Locate every blood parasite and identify its species.
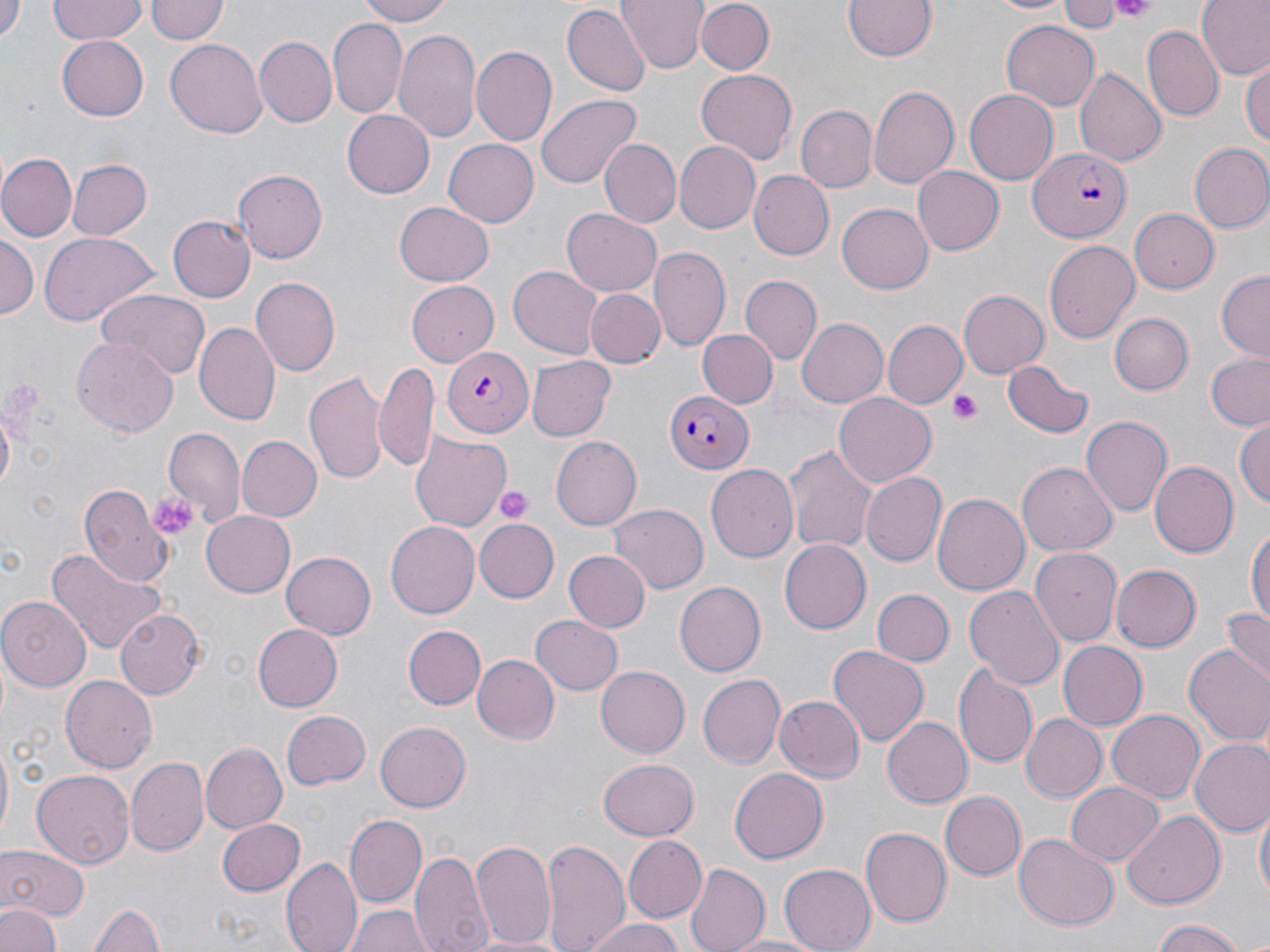
Approximate bounding boxes as named x1/y1/x2/y2 corners in pixels.
Plasmodium falciparum-infected red blood cells: (x1=1030, y1=149, x2=1130, y2=240), (x1=440, y1=349, x2=532, y2=436), (x1=661, y1=387, x2=753, y2=474).
No Plasmodium ovale, Plasmodium malariae, Plasmodium vivax, Babesia divergens, or Trypanosoma brucei observed.

Summary:
  - Uninfected red blood cell locations: (x1=0, y1=0, x2=23, y2=45), (x1=49, y1=0, x2=147, y2=44), (x1=145, y1=0, x2=226, y2=45), (x1=355, y1=0, x2=459, y2=26), (x1=617, y1=0, x2=705, y2=74), (x1=841, y1=0, x2=940, y2=63), (x1=980, y1=0, x2=1078, y2=15), (x1=1197, y1=0, x2=1269, y2=79), (x1=696, y1=1, x2=775, y2=74), (x1=1058, y1=1, x2=1122, y2=30), (x1=561, y1=5, x2=649, y2=95), (x1=330, y1=20, x2=406, y2=116), (x1=1001, y1=21, x2=1102, y2=110), (x1=1141, y1=25, x2=1225, y2=123), (x1=393, y1=28, x2=481, y2=144), (x1=56, y1=32, x2=149, y2=118), (x1=253, y1=36, x2=336, y2=126), (x1=165, y1=39, x2=266, y2=139), (x1=470, y1=45, x2=558, y2=146), (x1=1241, y1=61, x2=1269, y2=144), (x1=695, y1=68, x2=797, y2=163), (x1=1075, y1=68, x2=1166, y2=168), (x1=868, y1=85, x2=959, y2=190), (x1=963, y1=89, x2=1059, y2=184), (x1=536, y1=94, x2=643, y2=188), (x1=795, y1=106, x2=875, y2=194), (x1=341, y1=109, x2=434, y2=198), (x1=444, y1=137, x2=542, y2=227), (x1=599, y1=139, x2=681, y2=228), (x1=674, y1=141, x2=761, y2=232), (x1=1188, y1=143, x2=1270, y2=234), (x1=1, y1=155, x2=77, y2=240), (x1=66, y1=159, x2=151, y2=240), (x1=913, y1=167, x2=1003, y2=255), (x1=232, y1=169, x2=326, y2=264), (x1=748, y1=170, x2=834, y2=260), (x1=391, y1=201, x2=494, y2=286), (x1=836, y1=203, x2=932, y2=294), (x1=562, y1=208, x2=663, y2=296), (x1=1129, y1=208, x2=1219, y2=293), (x1=169, y1=215, x2=256, y2=301), (x1=39, y1=232, x2=158, y2=326), (x1=0, y1=233, x2=38, y2=320), (x1=1044, y1=239, x2=1140, y2=345), (x1=651, y1=247, x2=731, y2=351), (x1=509, y1=263, x2=604, y2=358), (x1=1216, y1=272, x2=1269, y2=360), (x1=740, y1=274, x2=822, y2=362), (x1=249, y1=275, x2=340, y2=379), (x1=406, y1=280, x2=499, y2=365), (x1=584, y1=288, x2=666, y2=368), (x1=99, y1=289, x2=209, y2=379), (x1=958, y1=289, x2=1050, y2=377), (x1=1109, y1=312, x2=1192, y2=394), (x1=797, y1=319, x2=888, y2=406), (x1=884, y1=321, x2=967, y2=408), (x1=195, y1=322, x2=280, y2=426), (x1=696, y1=329, x2=778, y2=409), (x1=71, y1=335, x2=179, y2=438), (x1=1205, y1=353, x2=1270, y2=431), (x1=528, y1=357, x2=614, y2=440), (x1=1001, y1=359, x2=1095, y2=439), (x1=375, y1=362, x2=435, y2=473), (x1=305, y1=369, x2=389, y2=483), (x1=833, y1=391, x2=936, y2=488), (x1=1082, y1=416, x2=1172, y2=517), (x1=1234, y1=418, x2=1270, y2=512), (x1=165, y1=429, x2=244, y2=527), (x1=410, y1=431, x2=511, y2=530), (x1=236, y1=435, x2=320, y2=521), (x1=549, y1=436, x2=642, y2=530), (x1=784, y1=443, x2=877, y2=554), (x1=1150, y1=460, x2=1239, y2=557), (x1=1017, y1=463, x2=1117, y2=555), (x1=708, y1=466, x2=799, y2=562), (x1=862, y1=472, x2=945, y2=565), (x1=76, y1=482, x2=169, y2=587), (x1=931, y1=492, x2=1030, y2=595), (x1=609, y1=505, x2=707, y2=593), (x1=200, y1=508, x2=296, y2=595), (x1=473, y1=517, x2=559, y2=602), (x1=386, y1=521, x2=480, y2=617), (x1=1246, y1=526, x2=1270, y2=632), (x1=780, y1=541, x2=871, y2=633), (x1=46, y1=546, x2=167, y2=657), (x1=1031, y1=547, x2=1122, y2=646), (x1=281, y1=550, x2=376, y2=638), (x1=565, y1=552, x2=649, y2=632), (x1=1111, y1=567, x2=1199, y2=651), (x1=675, y1=581, x2=765, y2=677), (x1=963, y1=583, x2=1064, y2=687), (x1=870, y1=588, x2=954, y2=667), (x1=0, y1=595, x2=91, y2=688), (x1=1222, y1=606, x2=1270, y2=685), (x1=115, y1=609, x2=205, y2=699), (x1=531, y1=614, x2=623, y2=694), (x1=254, y1=624, x2=342, y2=711), (x1=402, y1=624, x2=484, y2=711), (x1=1058, y1=639, x2=1146, y2=732), (x1=828, y1=645, x2=929, y2=746), (x1=1185, y1=645, x2=1270, y2=748), (x1=471, y1=654, x2=558, y2=744), (x1=954, y1=662, x2=1036, y2=769), (x1=595, y1=663, x2=689, y2=756), (x1=697, y1=674, x2=783, y2=770), (x1=62, y1=675, x2=159, y2=774), (x1=774, y1=695, x2=863, y2=783), (x1=281, y1=709, x2=369, y2=789), (x1=1107, y1=710, x2=1206, y2=803), (x1=1020, y1=714, x2=1108, y2=803), (x1=882, y1=716, x2=971, y2=808), (x1=375, y1=720, x2=470, y2=811), (x1=0, y1=740, x2=13, y2=844), (x1=1190, y1=740, x2=1270, y2=838), (x1=200, y1=743, x2=287, y2=834), (x1=127, y1=756, x2=208, y2=855), (x1=599, y1=758, x2=699, y2=839), (x1=730, y1=766, x2=830, y2=864), (x1=34, y1=770, x2=134, y2=868), (x1=1065, y1=780, x2=1165, y2=866), (x1=940, y1=792, x2=1027, y2=880), (x1=1256, y1=807, x2=1268, y2=905), (x1=1124, y1=810, x2=1225, y2=907), (x1=345, y1=814, x2=427, y2=906), (x1=215, y1=816, x2=305, y2=897), (x1=862, y1=827, x2=952, y2=927), (x1=1015, y1=833, x2=1118, y2=930), (x1=621, y1=834, x2=705, y2=923), (x1=541, y1=837, x2=630, y2=952), (x1=471, y1=838, x2=558, y2=951), (x1=0, y1=844, x2=91, y2=923), (x1=413, y1=847, x2=493, y2=952), (x1=282, y1=855, x2=360, y2=952), (x1=685, y1=862, x2=770, y2=952), (x1=779, y1=865, x2=875, y2=952), (x1=91, y1=899, x2=163, y2=952), (x1=0, y1=903, x2=61, y2=952), (x1=347, y1=904, x2=432, y2=952), (x1=585, y1=917, x2=685, y2=952), (x1=1150, y1=922, x2=1249, y2=952), (x1=722, y1=934, x2=828, y2=951)
  - Platelet locations: (x1=1112, y1=0, x2=1157, y2=20), (x1=950, y1=390, x2=982, y2=423), (x1=496, y1=485, x2=533, y2=525), (x1=147, y1=491, x2=196, y2=538)
  - Slide-level diagnosis: Plasmodium falciparum
  - Stain: May-Grünwald-Giemsa
  - Modality: optical microscopy
  - Magnification: 1000x
  - Preparation: thin blood smear
  - Image size: 1270×952 pixels
  - Field of view: one of a larger specimen